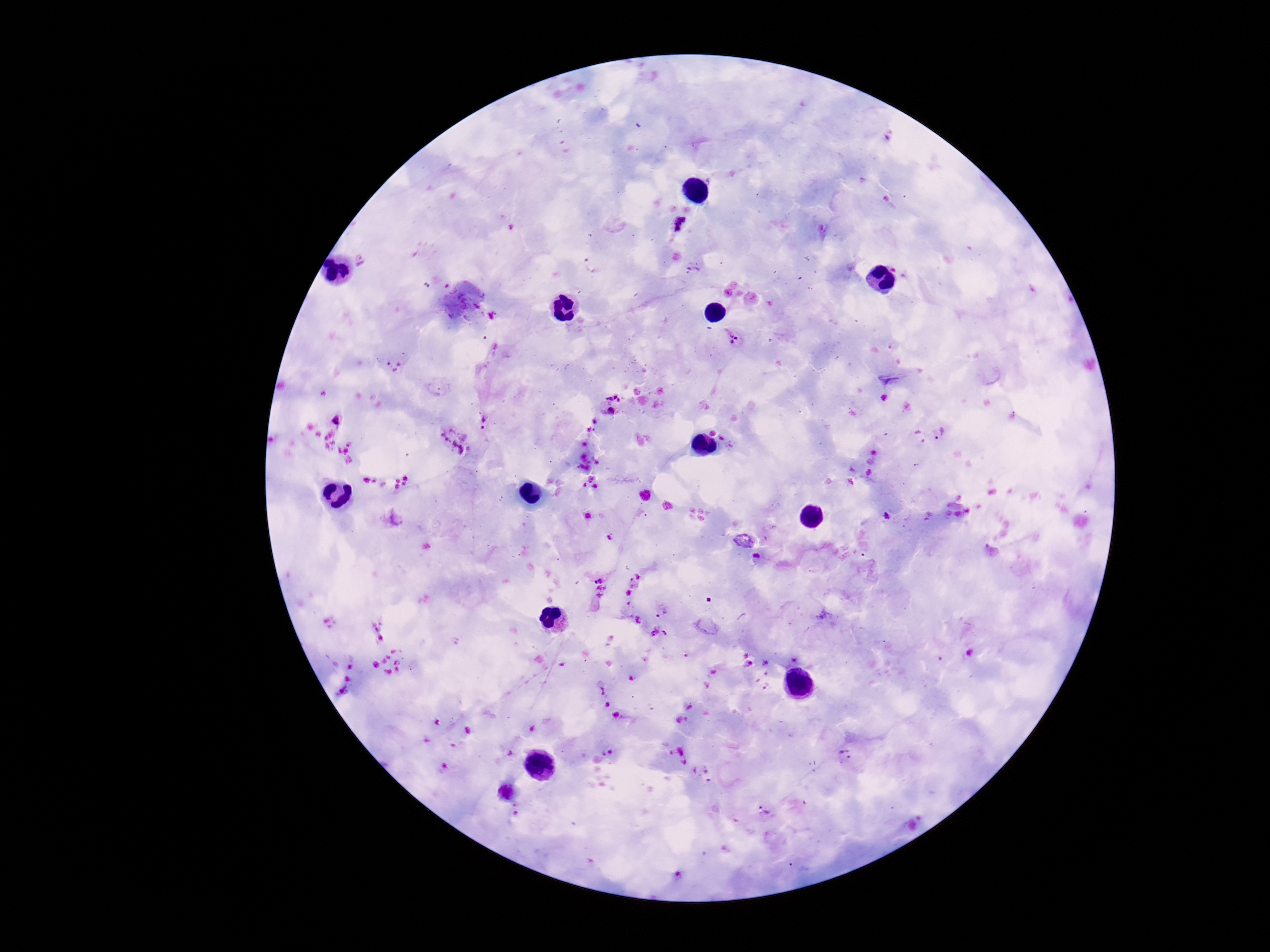

Approximate centers as [x, y] in pixels. Plasmodium parasite locations: [680, 226], [492, 316], [732, 339], [393, 365], [610, 404], [334, 419], [483, 422], [938, 433], [453, 442], [886, 517], [757, 557], [600, 572], [599, 592], [658, 633], [845, 757], [710, 776], [766, 812]. One field from this slide. Giemsa stain. Thick peripheral-blood smear. 100x magnification. Patient malaria status: positive. Image is 1270×952 pixels. Photographed through the microscope eyepiece with a smartphone camera.